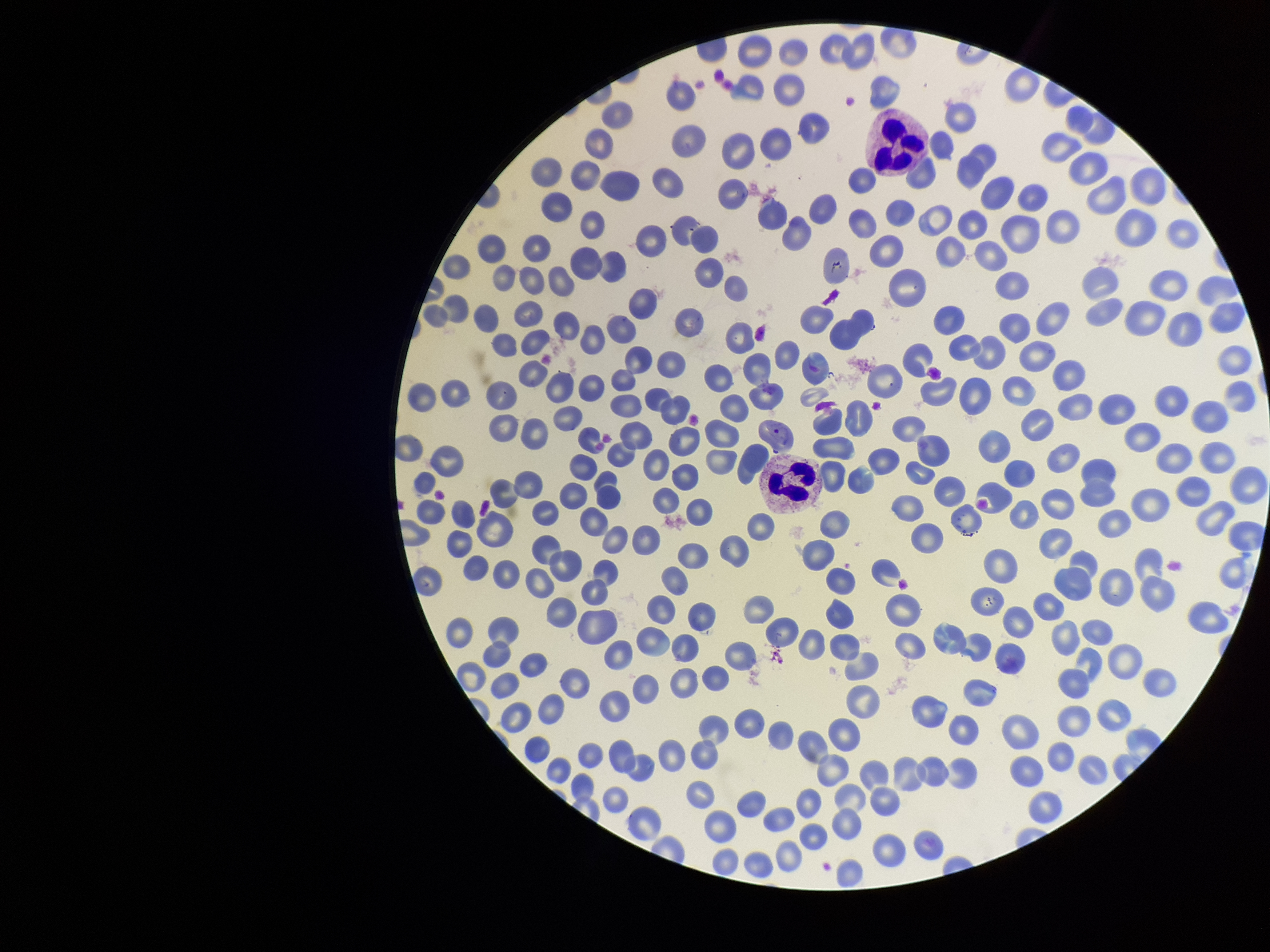

field of view = single
parasitized red blood cell count = 0
image size = 1270×952 pixels
patient malaria status = infected
parasitized red blood cells = none detected
red blood cell count = 277
species reported for this patient = Plasmodium vivax
preparation = thin smear
capture = smartphone photograph through the microscope eyepiece
stain = Giemsa